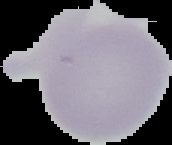

{
  "malaria_status": "uninfected",
  "image_size": "172×145 pixels",
  "preparation": "thin blood smear",
  "image_type": "cell region segmented out of the field of view; surrounding area masked to black"
}